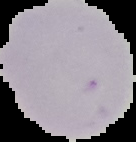
preparation = thin blood film
result = no malaria parasites seen
image type = cell region segmented out of the field of view; surrounding area masked to black
image size = 136×142 pixels